Classify this cell by malaria status.
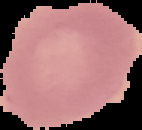
It is uninfected.

preparation = thin blood smear
image type = segmented cell region on a black background
image size = 142×130 pixels